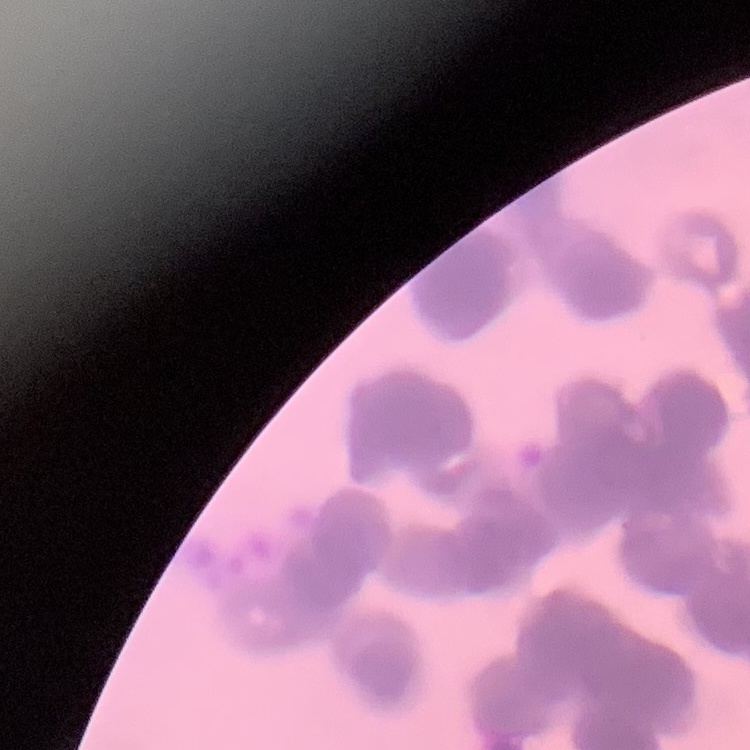

{
  "erythrocyte_morphology": "rouleaux formation",
  "image_type": "square crop of a larger photomicrograph",
  "stain": "Field's or Giemsa",
  "preparation": "thin blood smear"
}